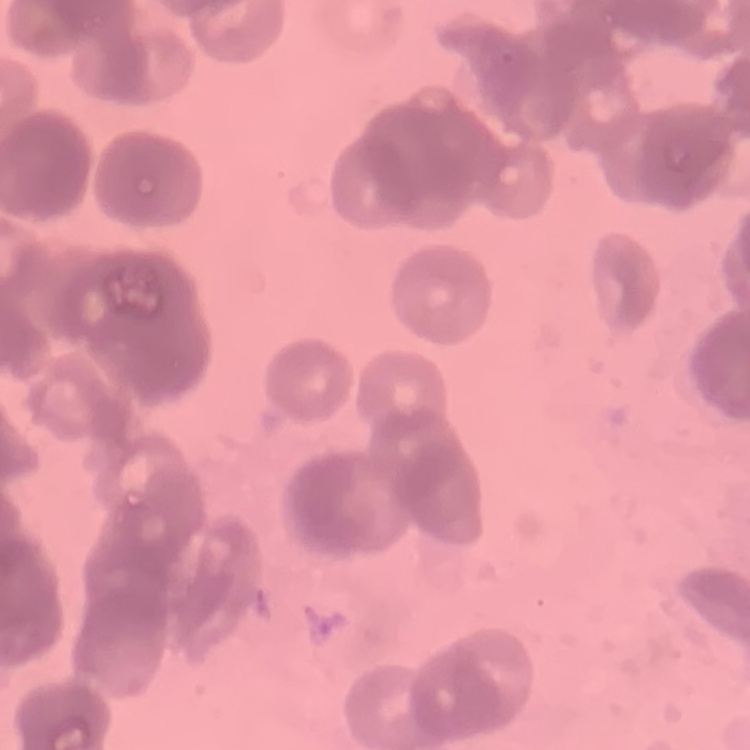
{
  "erythrocyte_morphology": "rouleaux formation",
  "stain": "Field's or Giemsa",
  "preparation": "thin peripheral smear",
  "image_type": "square crop of a larger photomicrograph"
}